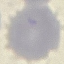
Summary:
  - Result: no malaria parasites detected
  - Preparation: thin smear
  - Capture: smartphone camera at the microscope eyepiece
  - Image type: cell patch, automatically extracted from a larger field of view and resized to 64 × 64 pixels
  - Stain: Giemsa